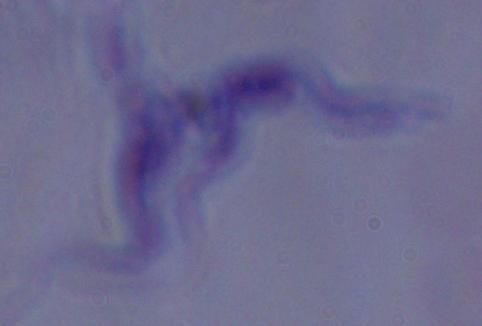
identification = trypanosome
modality = photomicrograph
magnification = 1000x